Describe the morphology of the erythrocytes.
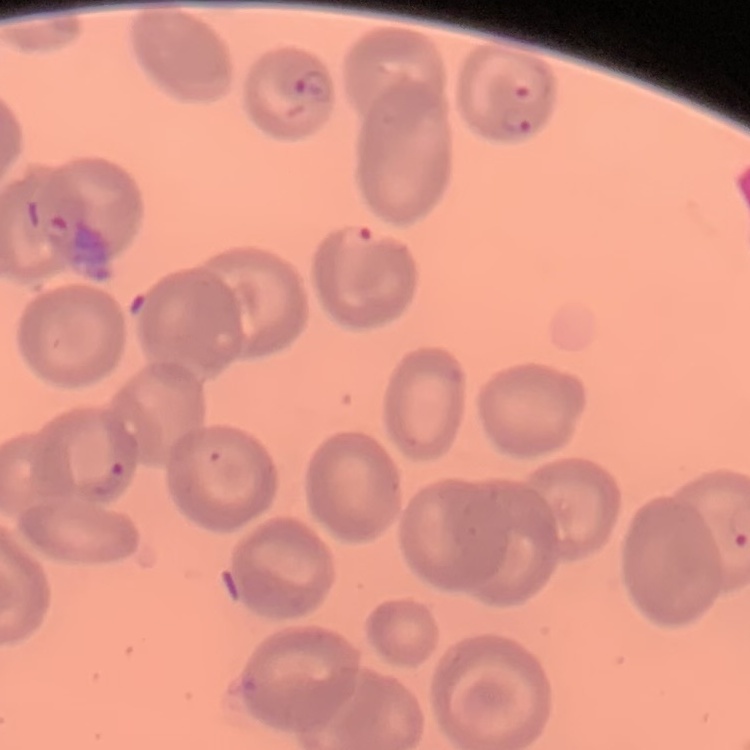

No rouleaux formation.

stain = Field's or Giemsa
preparation = thin peripheral smear
image type = square crop of a larger photomicrograph